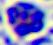

Summary:
  - Identification: leukocyte
  - Magnification: 400x
  - Modality: photomicrograph